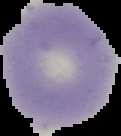

Summary:
  - Malaria status: uninfected
  - Preparation: thin blood smear
  - Image type: cell region segmented out of the field of view; surrounding area masked to black
  - Image size: 121×136 pixels